Assess this cell for malaria.
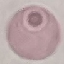

It is uninfected.

Giemsa stain. Thin blood smear. Photographed with a smartphone camera at the microscope eyepiece. Automatically extracted cell patch, resized to 64 × 64 pixels.